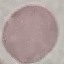
Summary:
  - Result: no malaria parasites detected
  - Capture: smartphone camera at the microscope eyepiece
  - Preparation: thin blood smear
  - Image type: cell patch, automatically extracted from a larger field of view and resized to 64 × 64 pixels
  - Stain: Giemsa